Report the malaria status of this cell.
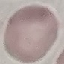
It is uninfected.

Summary:
  - Preparation: thin smear
  - Image type: cell patch, automatically extracted from a larger field of view and resized to 64 × 64 pixels
  - Capture: smartphone camera at the microscope eyepiece
  - Stain: Giemsa